Name the parasite shown.
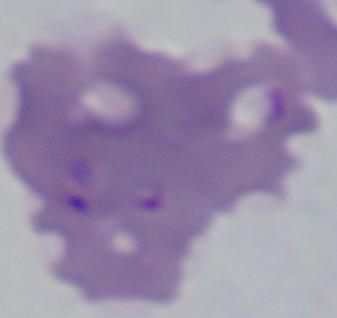
This is Babesia.

Photomicrograph. 1000x magnification.